Assess this cell for malaria.
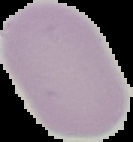

It is uninfected.

Image is 133×142 pixels. From a thin blood smear. Segmented cell region on a black background.